Assess the morphology of the erythrocytes.
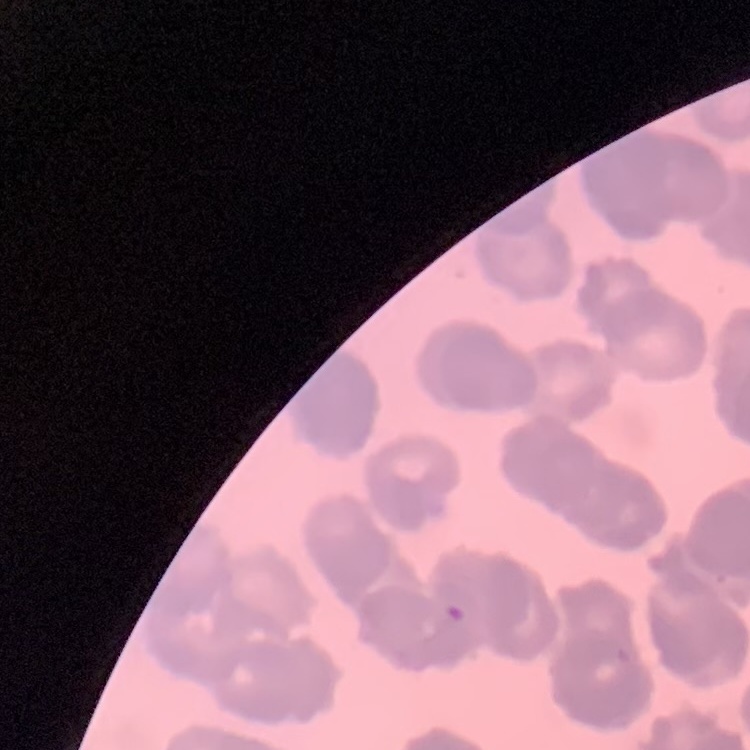

They show rouleaux formation.

Summary:
  - Preparation: thin peripheral smear
  - Image type: one tile cut from a larger photomicrograph
  - Stain: Field's or Giemsa